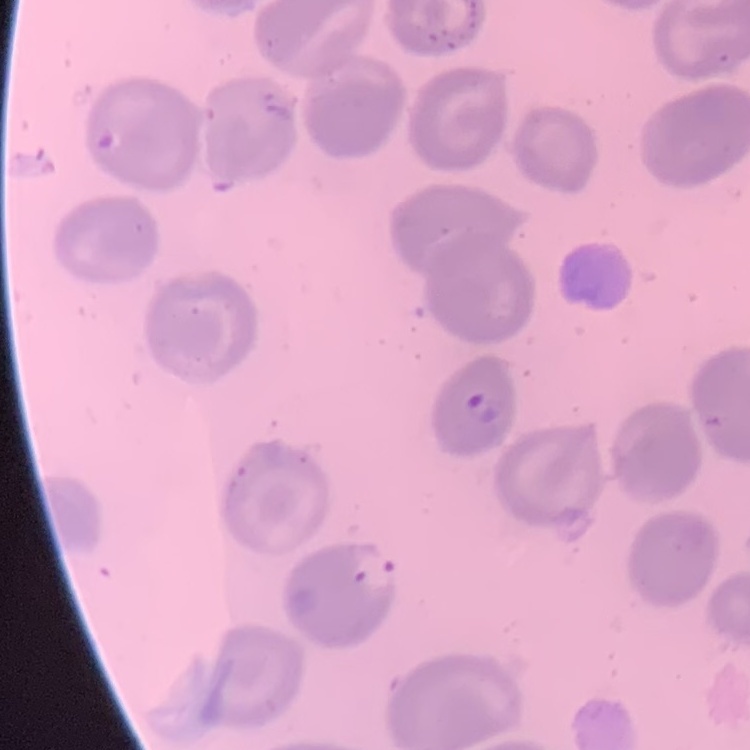

{
  "erythrocyte_morphology": "no rouleaux formation",
  "image_type": "square crop of a larger photomicrograph",
  "stain": "Field's or Giemsa",
  "preparation": "thin blood smear"
}